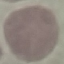

malaria status = uninfected
preparation = thin blood film
stain = Giemsa
image type = cell patch, automatically extracted from a larger field of view and resized to 64 × 64 pixels
capture = smartphone through the microscope eyepiece